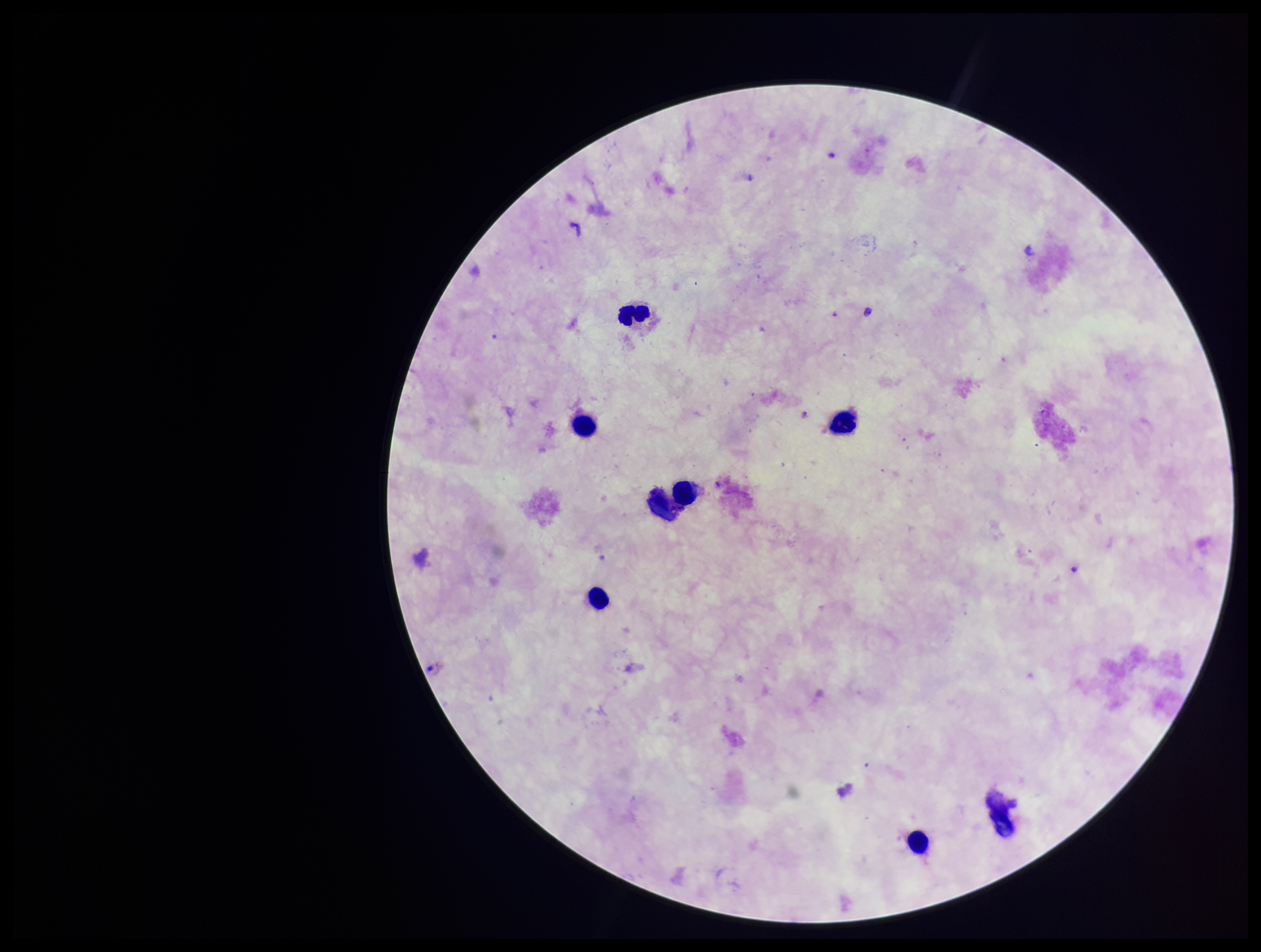

Parasite count: 0. One field from this slide. Leukocyte count: 6. Giemsa stain. Plasmodium parasites: none seen. Preparation: thick smear. Photographed through the microscope eyepiece with a smartphone camera. Image is 1261×952 pixels. Patient malaria status: negative.